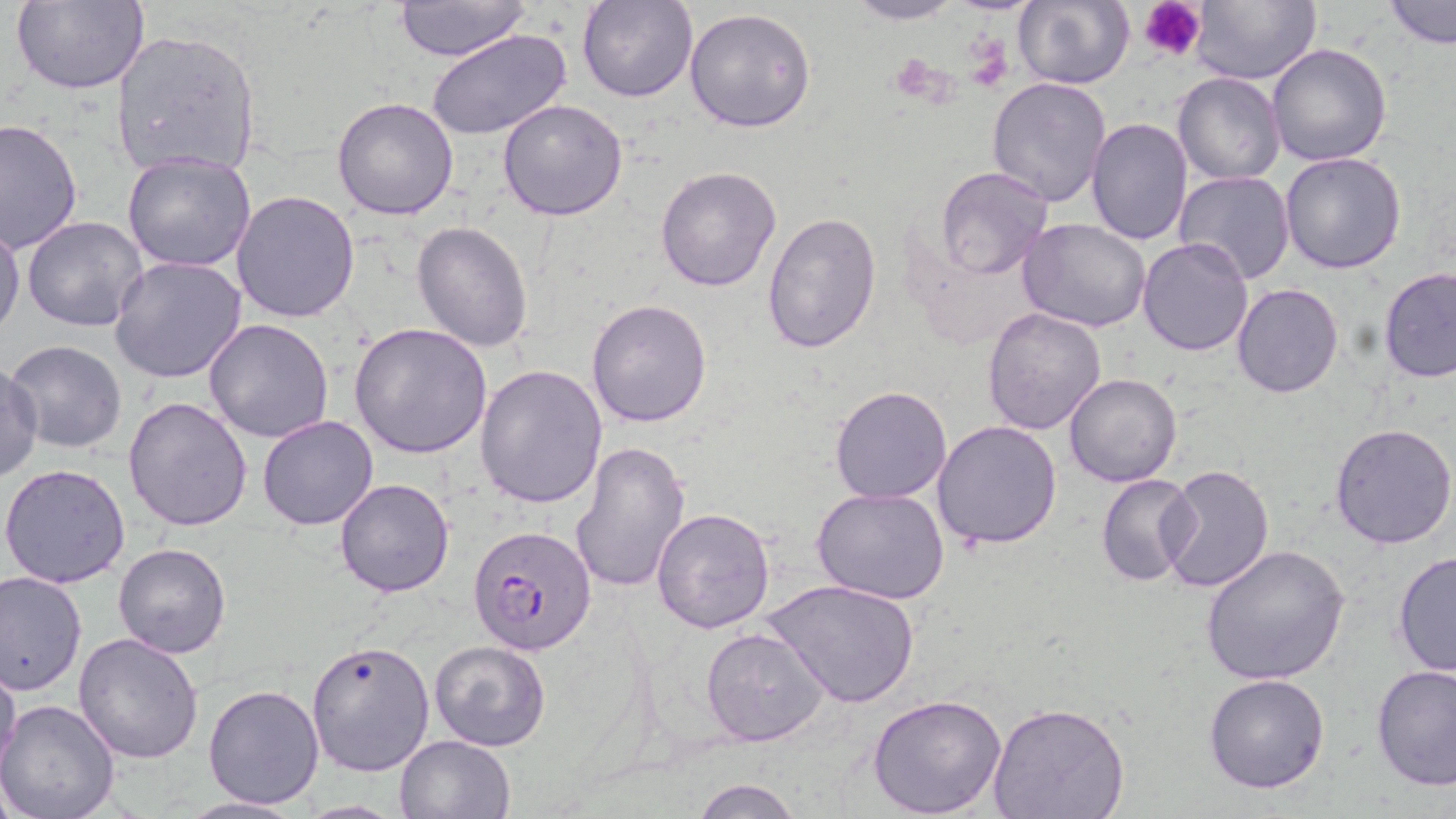
Summary:
  - Coordinate format: approximate bounding boxes as (x1,y1)-(x2,y2) corner pairs in pixels
  - Platelet locations: (1140,0)-(1207,61), (964,39)-(1008,88), (890,55)-(948,103)
  - Uninfected red blood cell locations: (391,0)-(533,64), (577,0)-(699,103), (841,0)-(968,25), (1012,0)-(1134,89), (1191,0)-(1320,85), (1384,0)-(1456,48), (9,1)-(149,94), (685,6)-(817,133), (427,28)-(575,143), (110,30)-(262,177), (1267,43)-(1394,167), (1173,73)-(1284,184), (987,77)-(1113,207), (332,98)-(459,221), (498,98)-(630,221), (1085,117)-(1193,245), (1,118)-(83,252), (122,152)-(257,274), (1279,153)-(1407,274), (655,165)-(783,292), (934,166)-(1053,280), (1172,170)-(1296,285), (231,190)-(362,323), (761,212)-(882,355), (22,217)-(148,332), (1016,219)-(1153,333), (411,220)-(532,353), (0,221)-(25,342), (1137,236)-(1253,356), (110,257)-(248,385), (1377,267)-(1456,383), (1231,283)-(1345,400), (586,298)-(714,428), (981,306)-(1107,436), (203,318)-(333,443), (349,322)-(493,459), (5,340)-(127,454), (0,363)-(43,481), (474,364)-(607,509), (1063,373)-(1183,489), (830,387)-(951,503), (124,394)-(253,531), (257,415)-(378,531), (933,421)-(1064,549), (1330,424)-(1456,550), (569,439)-(690,596), (1158,462)-(1275,595), (0,463)-(133,588), (1095,474)-(1199,587), (334,478)-(454,597), (811,488)-(951,606), (651,507)-(776,634), (113,541)-(232,659), (1202,544)-(1351,686), (1392,549)-(1455,680), (1,571)-(87,694), (765,579)-(920,707), (701,626)-(828,747), (73,631)-(204,762), (306,638)-(437,777), (430,640)-(550,751), (0,654)-(22,779), (1371,663)-(1456,790), (1202,672)-(1331,793), (203,683)-(326,810), (866,693)-(1008,817), (0,699)-(122,819), (987,701)-(1129,819), (395,733)-(515,818), (691,778)-(802,818), (179,795)-(307,818)
  - Plasmodium falciparum-infected red blood cell locations: (470,524)-(599,655)
  - Slide-level diagnosis: Plasmodium falciparum
  - Field of view: single
  - Modality: light microscopy
  - Image size: 1456×819 pixels
  - Preparation: thin blood smear
  - Magnification: 1000x
  - Stain: May-Grünwald-Giemsa